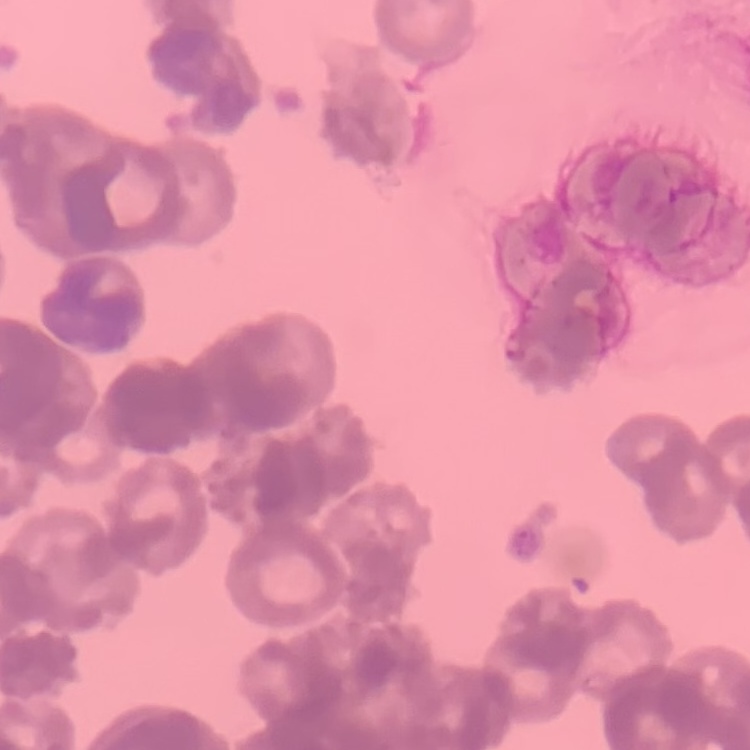

Summary:
  - Erythrocyte morphology: rouleaux formation
  - Image type: square crop of a larger photomicrograph
  - Preparation: thin peripheral smear
  - Stain: Field's or Giemsa